Name the parasite shown.
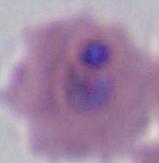

This is Plasmodium.

Summary:
  - Modality: photomicrograph
  - Magnification: 400x or 1000x